Classify this cell by malaria status.
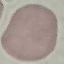
Uninfected.

preparation = thin blood smear
capture = smartphone camera at the microscope eyepiece
stain = Giemsa
image type = cell patch, automatically extracted from a larger field of view and resized to 64 × 64 pixels